Describe the morphology of the erythrocytes.
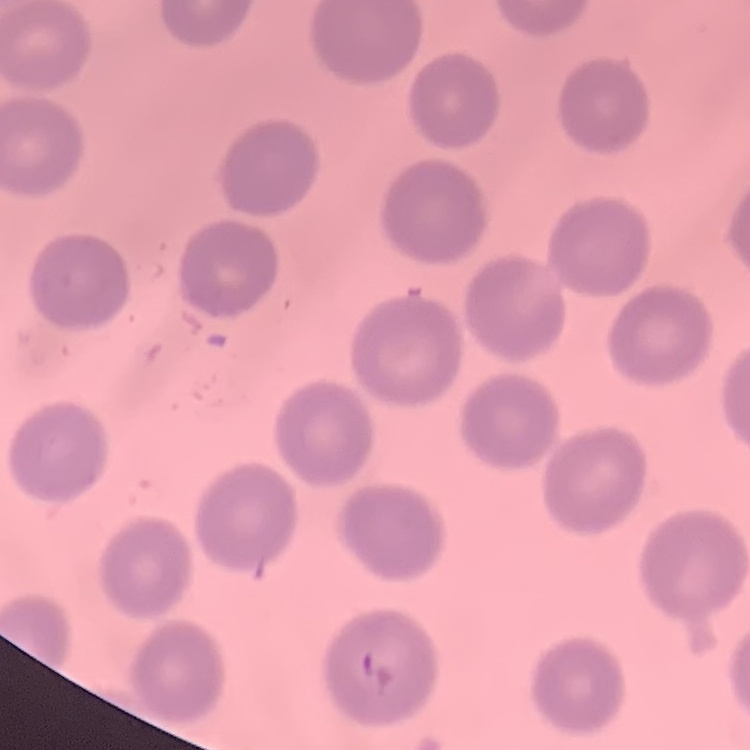

They show no rouleaux formation.

Square crop of a larger photomicrograph. Stained with either Field's or Giemsa. Thin blood film.